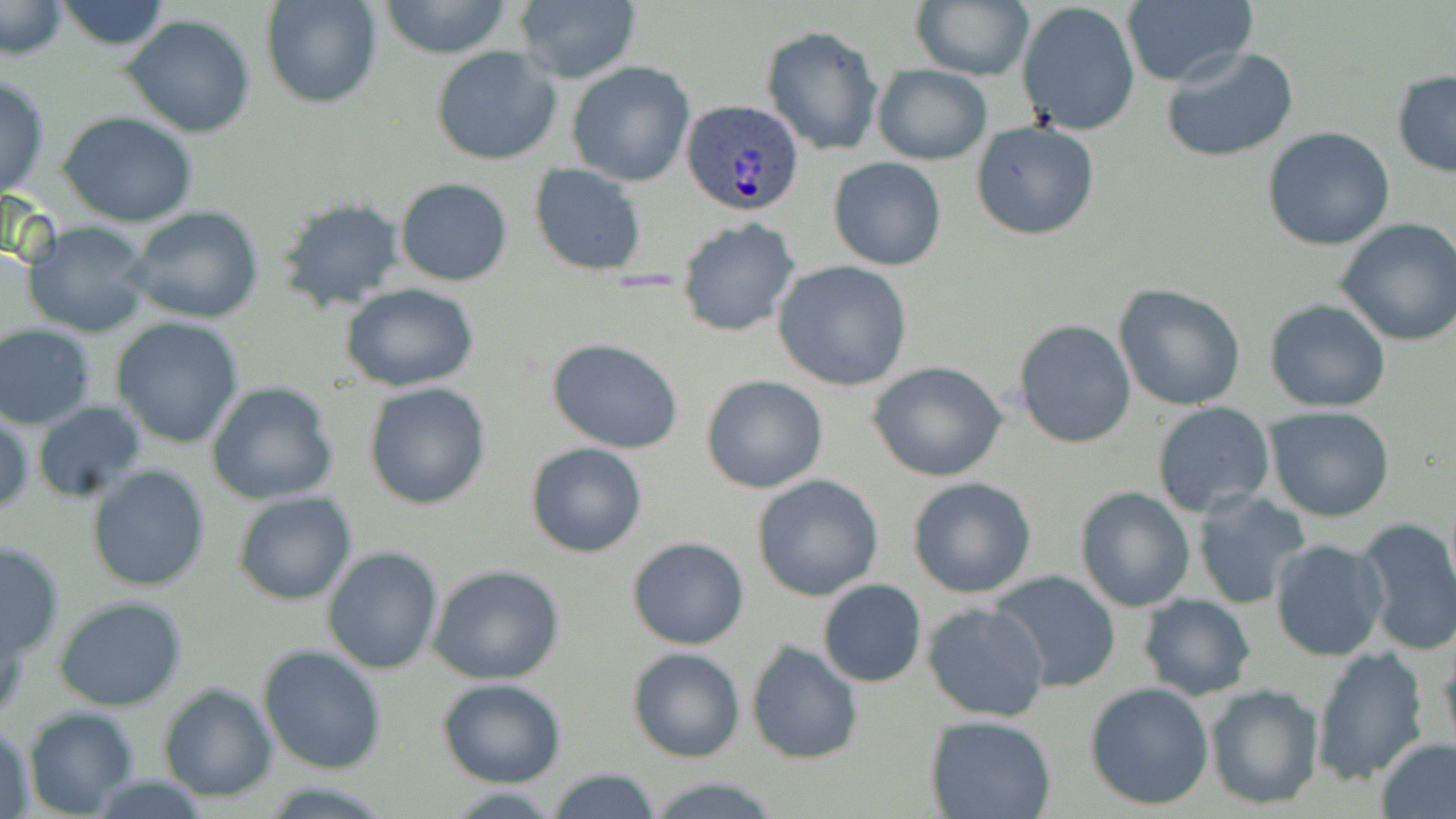
Approximate bounding boxes as (x1,y1)-(x2,y2) corner pairs in pixels. Uninfected red blood cell locations: (53,0)-(171,52), (259,0)-(383,110), (376,0)-(516,60), (511,0)-(641,85), (1,1)-(68,60), (911,1)-(1034,81), (1017,2)-(1143,138), (1120,2)-(1257,87), (122,15)-(257,138), (762,24)-(885,156), (430,46)-(562,167), (1160,46)-(1301,164), (567,61)-(695,187), (871,64)-(992,165), (1391,71)-(1456,177), (0,75)-(51,200), (59,110)-(199,228), (971,119)-(1101,241), (1261,126)-(1395,250), (828,157)-(947,270), (529,165)-(648,276), (395,177)-(514,286), (275,198)-(408,315), (125,205)-(265,324), (677,217)-(802,338), (1335,219)-(1456,347), (22,220)-(155,338), (771,260)-(915,392), (1113,283)-(1246,411), (340,284)-(482,392), (1265,299)-(1390,414), (110,317)-(244,448), (1013,319)-(1138,449), (0,324)-(96,431), (547,338)-(685,454), (867,361)-(1009,482), (701,374)-(828,494), (205,380)-(339,505), (363,382)-(493,510), (34,402)-(148,505), (1151,403)-(1274,519), (1264,406)-(1396,523), (0,410)-(33,518), (525,441)-(647,559), (87,463)-(211,592), (753,474)-(884,602), (907,477)-(1037,599), (1076,487)-(1195,612), (1190,490)-(1312,610), (232,491)-(357,606), (1351,517)-(1456,657), (626,536)-(750,650), (1270,538)-(1391,662), (1,539)-(65,661), (322,546)-(444,675), (426,564)-(567,684), (989,569)-(1123,693), (818,579)-(926,687), (54,594)-(189,711), (1137,594)-(1256,700), (923,603)-(1051,723), (1438,636)-(1456,757), (746,638)-(864,765), (257,644)-(386,775), (627,645)-(746,763), (1310,649)-(1427,785), (437,678)-(565,787), (1085,681)-(1215,810), (158,683)-(278,802), (1204,683)-(1323,809), (23,707)-(140,817), (926,714)-(1056,818), (2,720)-(37,818), (1376,737)-(1456,819), (544,766)-(662,819), (646,776)-(784,817). Plasmodium ovale-infected red blood cell locations: (679,99)-(805,218). Slide-level diagnosis: Plasmodium ovale. 1000x magnification. May-Grünwald-Giemsa stain. Thin blood smear. Optical microscopy. Image is 1456×819 pixels. One field of a larger specimen.